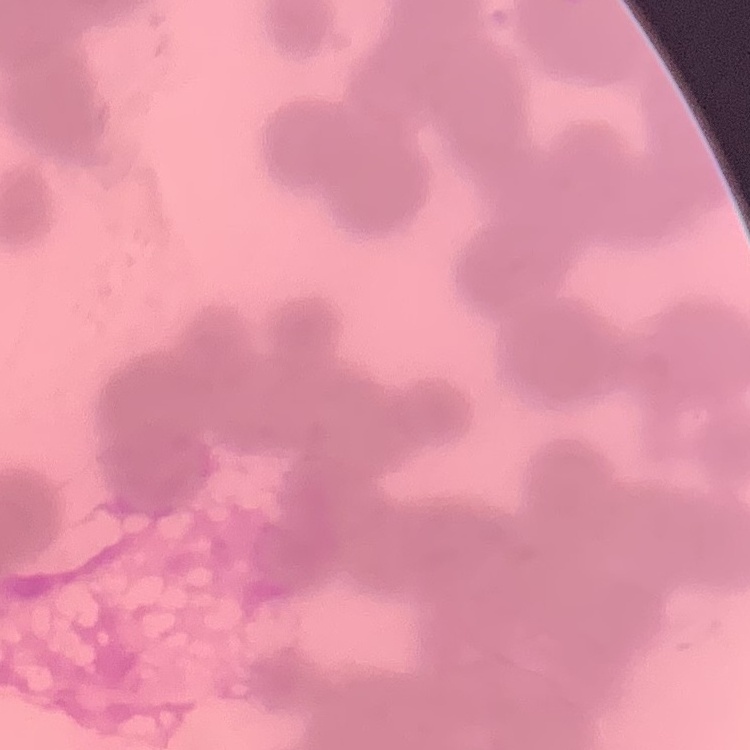
Summary:
  - Erythrocyte morphology: rouleaux formation
  - Image type: one tile cut from a larger photomicrograph
  - Stain: Field's or Giemsa
  - Preparation: thin peripheral smear